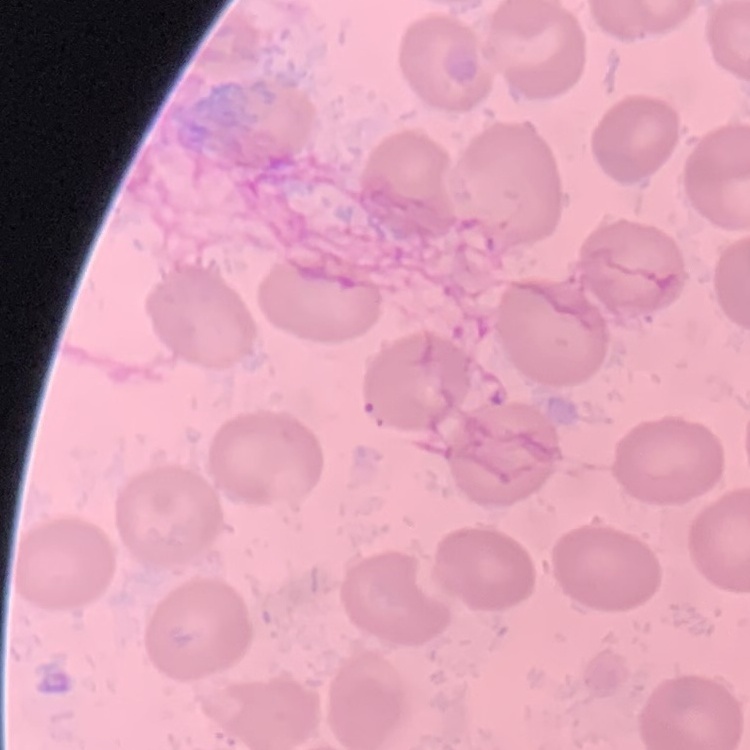

red blood cell morphology = no rouleaux formation
image type = one tile cut from a larger photomicrograph
preparation = thin blood smear
stain = Field's or Giemsa